Assess this cell for malaria.
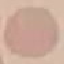

Uninfected.

preparation = thin blood film
stain = Giemsa
image type = cell patch, automatically extracted from a larger field of view and resized to 64 × 64 pixels
capture = smartphone camera at the microscope eyepiece